Classify this cell by malaria status.
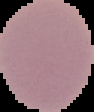
It is uninfected.

{
  "image_size": "94×112 pixels",
  "preparation": "thin blood smear",
  "image_type": "segmented cell region on a black background"
}